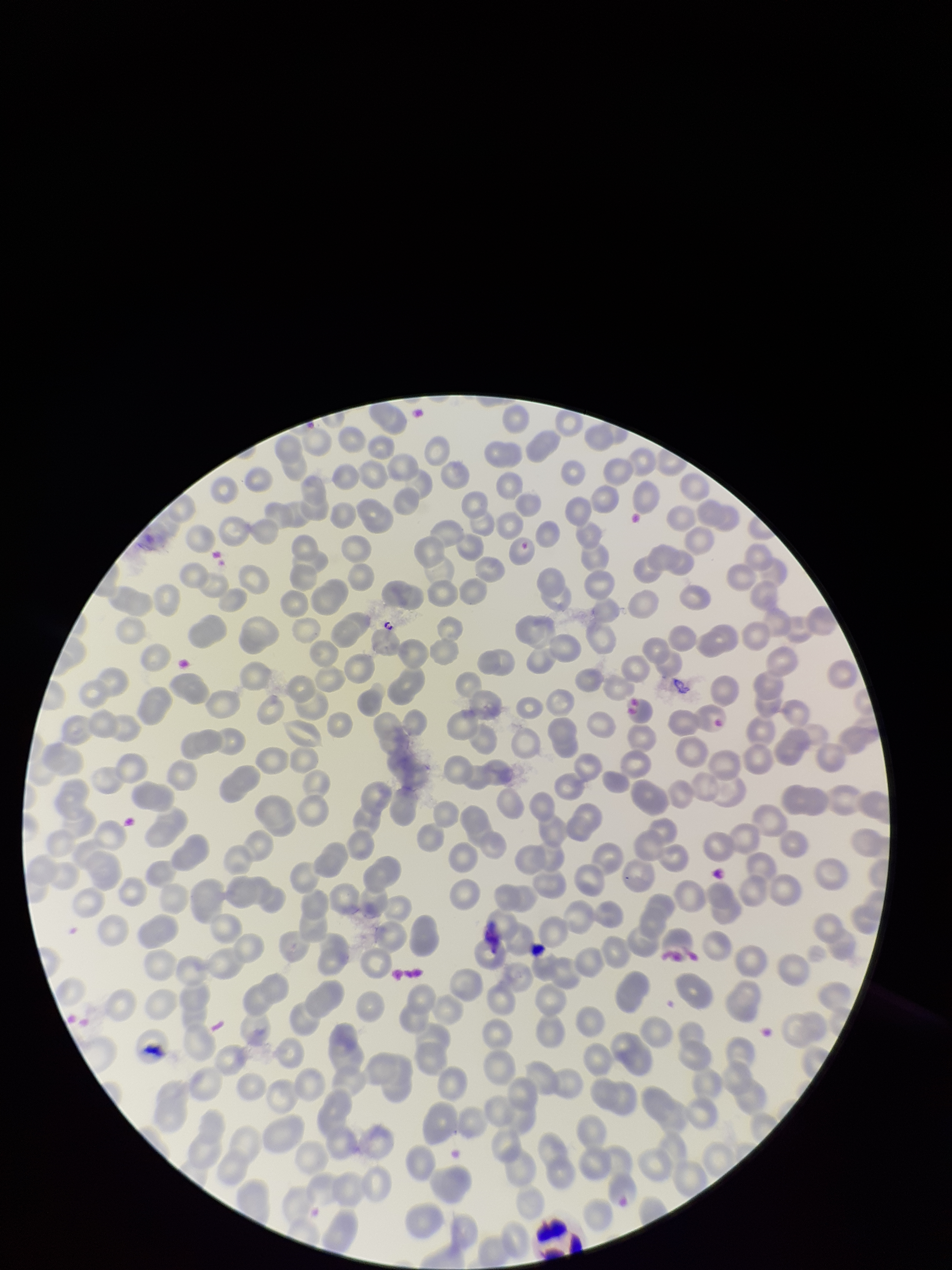
Summary:
  - Stain: Giemsa
  - Patient malaria status: negative
  - Capture: smartphone photograph through the microscope eyepiece
  - Parasitized red blood cells: none identified
  - Preparation: thin
  - Image size: 952×1270 pixels
  - Red blood cell count: 274
  - Parasitized red blood cell count: 0
  - Field of view: one from this slide